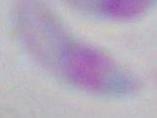

magnification = 1000x
modality = micrograph
identification = Toxoplasma gondii